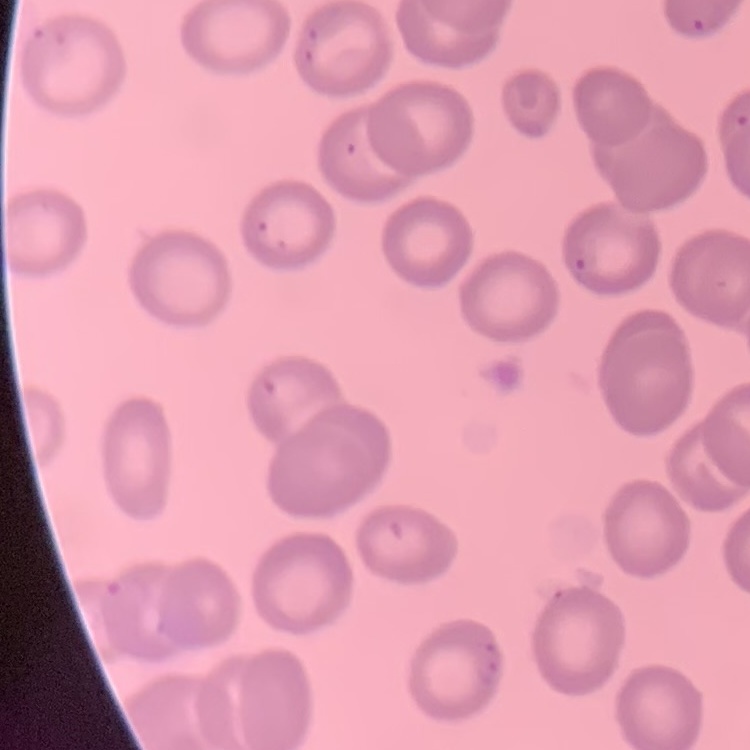
red_blood_cell_morphology: no rouleaux formation
preparation: thin peripheral smear
stain: Field's or Giemsa
image_type: one tile cut from a larger photomicrograph